Locate cells.
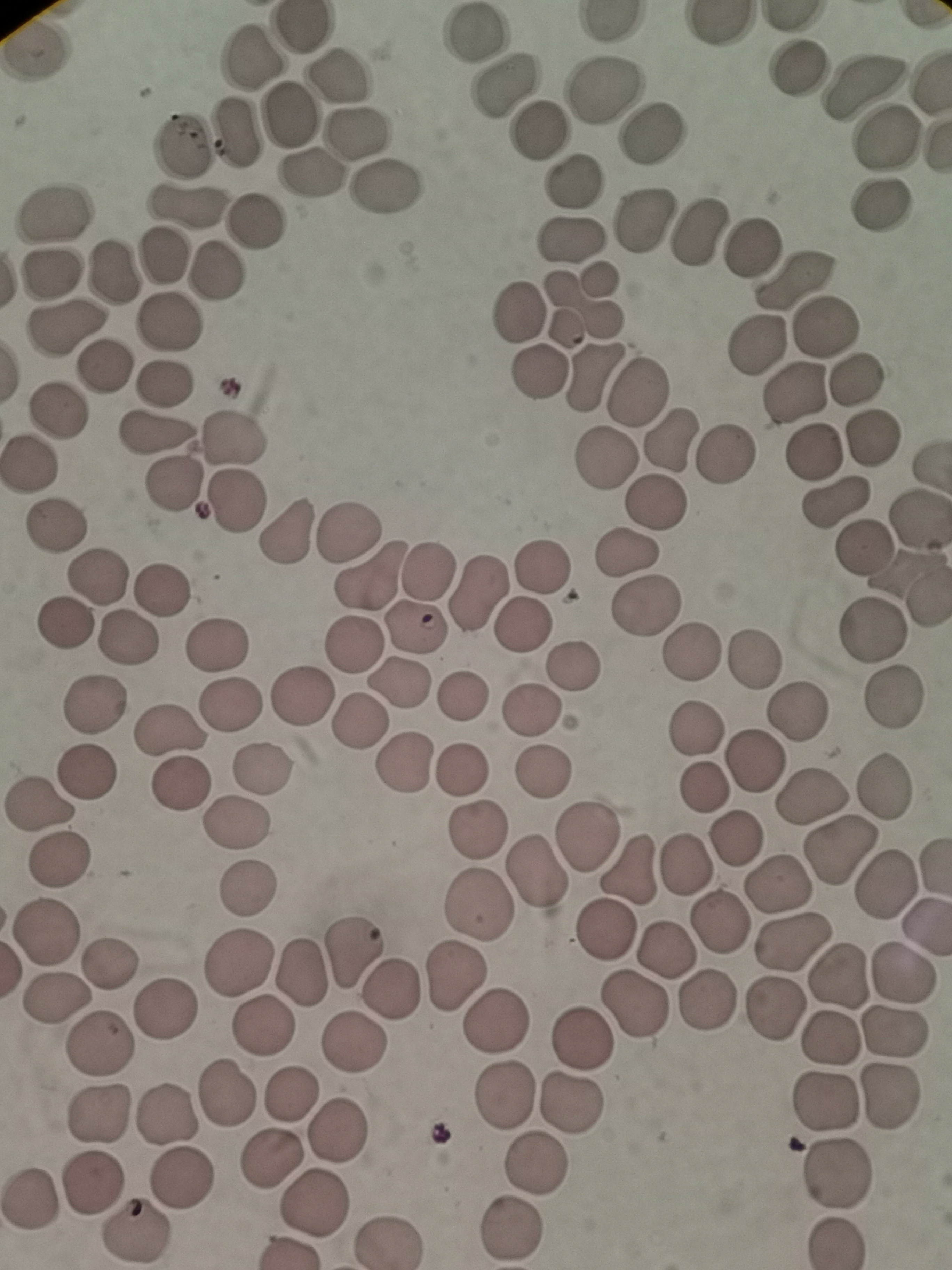

Approximate object centers, in pixels from the top-left corner.
Cells: (x=305, y=30), (x=475, y=35), (x=251, y=60), (x=794, y=68), (x=344, y=79), (x=859, y=84), (x=508, y=87), (x=602, y=91), (x=291, y=113), (x=235, y=133), (x=539, y=133), (x=649, y=133), (x=357, y=134), (x=883, y=139), (x=185, y=146), (x=313, y=171), (x=575, y=182), (x=390, y=184), (x=183, y=202), (x=881, y=205), (x=55, y=214), (x=256, y=222), (x=644, y=222), (x=700, y=231), (x=571, y=236), (x=749, y=248), (x=160, y=254), (x=115, y=269), (x=214, y=273), (x=51, y=278), (x=597, y=279), (x=797, y=281), (x=521, y=313), (x=172, y=324), (x=825, y=326), (x=63, y=328), (x=566, y=328), (x=757, y=344), (x=98, y=360), (x=540, y=372), (x=592, y=376), (x=856, y=381), (x=164, y=388), (x=794, y=391), (x=636, y=393), (x=52, y=413), (x=155, y=435), (x=234, y=436), (x=873, y=438), (x=671, y=439), (x=811, y=452), (x=724, y=456), (x=607, y=460), (x=30, y=462), (x=173, y=486), (x=236, y=500), (x=655, y=500), (x=837, y=503), (x=57, y=522), (x=287, y=532), (x=346, y=533), (x=864, y=546), (x=626, y=554), (x=537, y=567), (x=430, y=568), (x=370, y=575), (x=97, y=576), (x=477, y=590), (x=161, y=591), (x=642, y=605), (x=64, y=622), (x=418, y=628), (x=524, y=628), (x=871, y=632), (x=130, y=640), (x=356, y=641), (x=214, y=644), (x=694, y=649), (x=753, y=658), (x=578, y=668), (x=396, y=685), (x=465, y=694), (x=300, y=696), (x=891, y=696), (x=232, y=702), (x=94, y=704), (x=795, y=707), (x=530, y=711), (x=360, y=722), (x=693, y=727), (x=169, y=732), (x=753, y=763), (x=405, y=764), (x=262, y=767), (x=460, y=770), (x=545, y=771), (x=86, y=772), (x=181, y=782), (x=698, y=788), (x=885, y=789), (x=812, y=799), (x=38, y=806), (x=237, y=824), (x=475, y=827), (x=587, y=837), (x=734, y=837), (x=839, y=851), (x=57, y=862), (x=683, y=866), (x=629, y=869), (x=537, y=872), (x=884, y=885), (x=246, y=886), (x=781, y=886), (x=477, y=904), (x=717, y=924), (x=603, y=930), (x=45, y=931), (x=795, y=942), (x=354, y=950), (x=663, y=950), (x=108, y=965), (x=296, y=973), (x=840, y=975), (x=904, y=975), (x=452, y=976), (x=389, y=989), (x=58, y=996), (x=708, y=999), (x=633, y=1005), (x=164, y=1010), (x=777, y=1012), (x=495, y=1020), (x=263, y=1028), (x=892, y=1029), (x=829, y=1036), (x=582, y=1037), (x=352, y=1042), (x=98, y=1045), (x=290, y=1093), (x=503, y=1093), (x=223, y=1094), (x=889, y=1095), (x=827, y=1100), (x=567, y=1103), (x=96, y=1114), (x=164, y=1114), (x=337, y=1129), (x=535, y=1166), (x=834, y=1174), (x=181, y=1175), (x=91, y=1180), (x=30, y=1201), (x=314, y=1205), (x=508, y=1230), (x=133, y=1231), (x=386, y=1239), (x=837, y=1244).

Summary:
  - Field of view: single
  - Stain: Giemsa
  - Preparation: thin blood smear
  - Image size: 952×1270 pixels
  - Capture: smartphone camera at the microscope eyepiece